Give the position of every Plasmodium parasite.
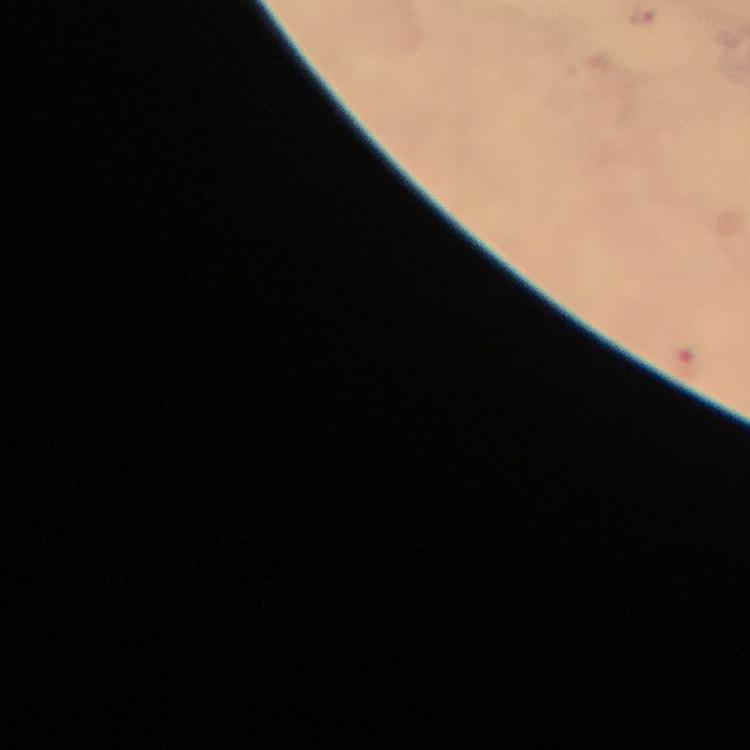

Approximate object centers, in pixels from the top-left corner.
Plasmodium parasites: (x=643, y=15).

Image is 750×750 pixels. Smartphone photograph taken through a microscope. Immersion oil applied. Cropped region of a single field of view. Thick blood smear. From a diagnostic examination for malaria. Giemsa stain. 100x magnification.